Classify this cell by malaria status.
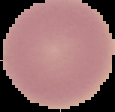
It is uninfected.

Summary:
  - Preparation: thin blood film
  - Image size: 115×112 pixels
  - Image type: segmented cell region with the area outside set to black